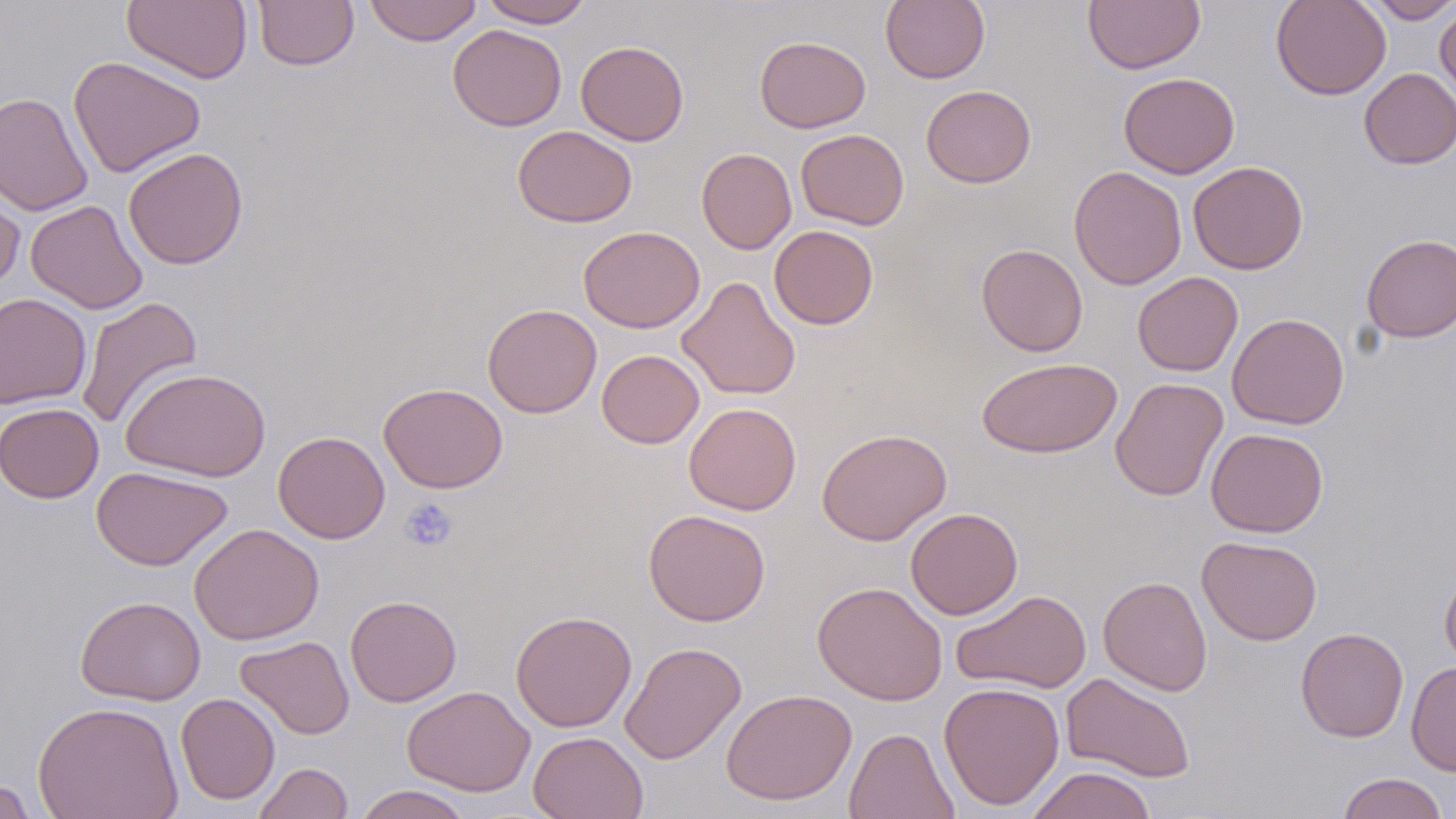 Approximate bounding boxes as (x1,y1)-(x2,y2) corner pairs in pixels. Uninfected red blood cell locations: (121,0)-(253,84), (253,0)-(359,71), (364,0)-(483,46), (478,0)-(594,27), (880,0)-(990,84), (1271,0)-(1391,100), (1364,0)-(1456,23), (1084,1)-(1205,74), (1435,5)-(1456,108), (447,24)-(567,131), (754,35)-(871,133), (575,40)-(689,146), (68,56)-(206,178), (1359,68)-(1456,169), (1118,72)-(1240,179), (921,85)-(1036,188), (0,91)-(94,216), (512,125)-(638,227), (795,129)-(909,230), (123,147)-(248,270), (696,147)-(797,254), (1188,160)-(1308,275), (1068,165)-(1187,290), (0,173)-(26,293), (25,200)-(148,314), (578,225)-(705,333), (769,225)-(878,329), (1361,234)-(1456,342), (976,244)-(1087,357), (1132,271)-(1243,376), (677,276)-(801,401), (0,292)-(91,409), (76,295)-(203,430), (482,303)-(601,418), (1227,313)-(1349,430), (597,349)-(704,448), (978,357)-(1121,458), (120,366)-(271,482), (1110,377)-(1229,501), (378,382)-(508,493), (0,402)-(103,503), (683,402)-(801,515), (816,428)-(952,546), (1206,428)-(1328,537), (273,430)-(390,544), (91,465)-(232,570), (905,507)-(1023,620), (643,509)-(771,626), (189,523)-(324,645), (1197,535)-(1322,645), (1440,565)-(1456,670), (1098,575)-(1212,696), (812,581)-(948,705), (951,589)-(1091,694), (75,595)-(206,706), (345,595)-(462,707), (510,610)-(637,732), (1295,627)-(1409,742), (235,635)-(355,740), (620,641)-(746,764), (1406,662)-(1456,776), (1061,672)-(1196,783), (939,681)-(1065,810), (402,686)-(535,796), (721,688)-(857,806), (176,692)-(280,804), (33,701)-(183,819), (843,727)-(960,819), (528,731)-(648,819), (252,762)-(353,819), (1026,766)-(1157,819), (1336,771)-(1450,819), (0,778)-(40,818), (353,785)-(474,819). Platelet locations: (399,497)-(458,552). Slide-level diagnosis: no evidence of blood parasites. Captured at 1000x magnification. Single field of view. Thin blood smear. Image is 1456×819 pixels. May-Grünwald-Giemsa stain. Light microscopy.